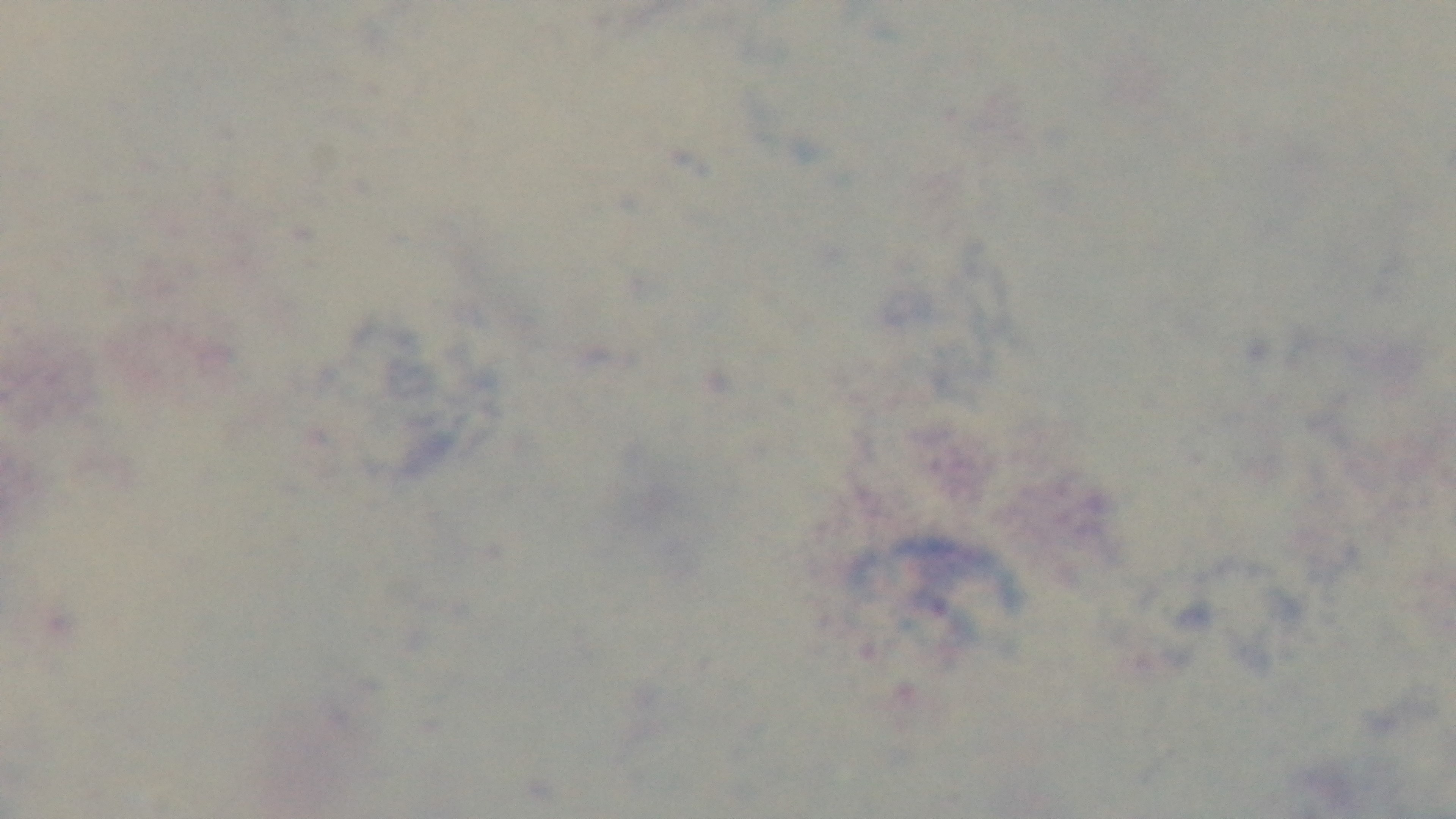

field_of_view: one from the slide
modality: light microscopy
malaria_status: negative
stain: Giemsa
objective: 100x oil immersion
preparation: thick smear
capture: mounted 4K digital camera